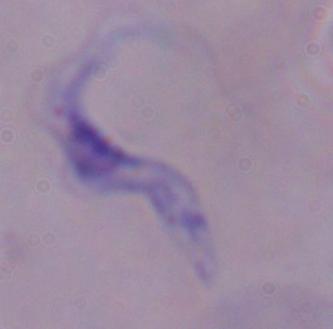 A trypanosome is seen. 1000x magnification. Photomicrograph.